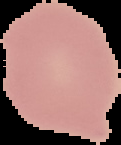
image size = 121×145 pixels
image type = cell region segmented out of the field of view; surrounding area masked to black
malaria status = uninfected
preparation = thin blood smear